Locate every malaria parasite and every leukocyte.
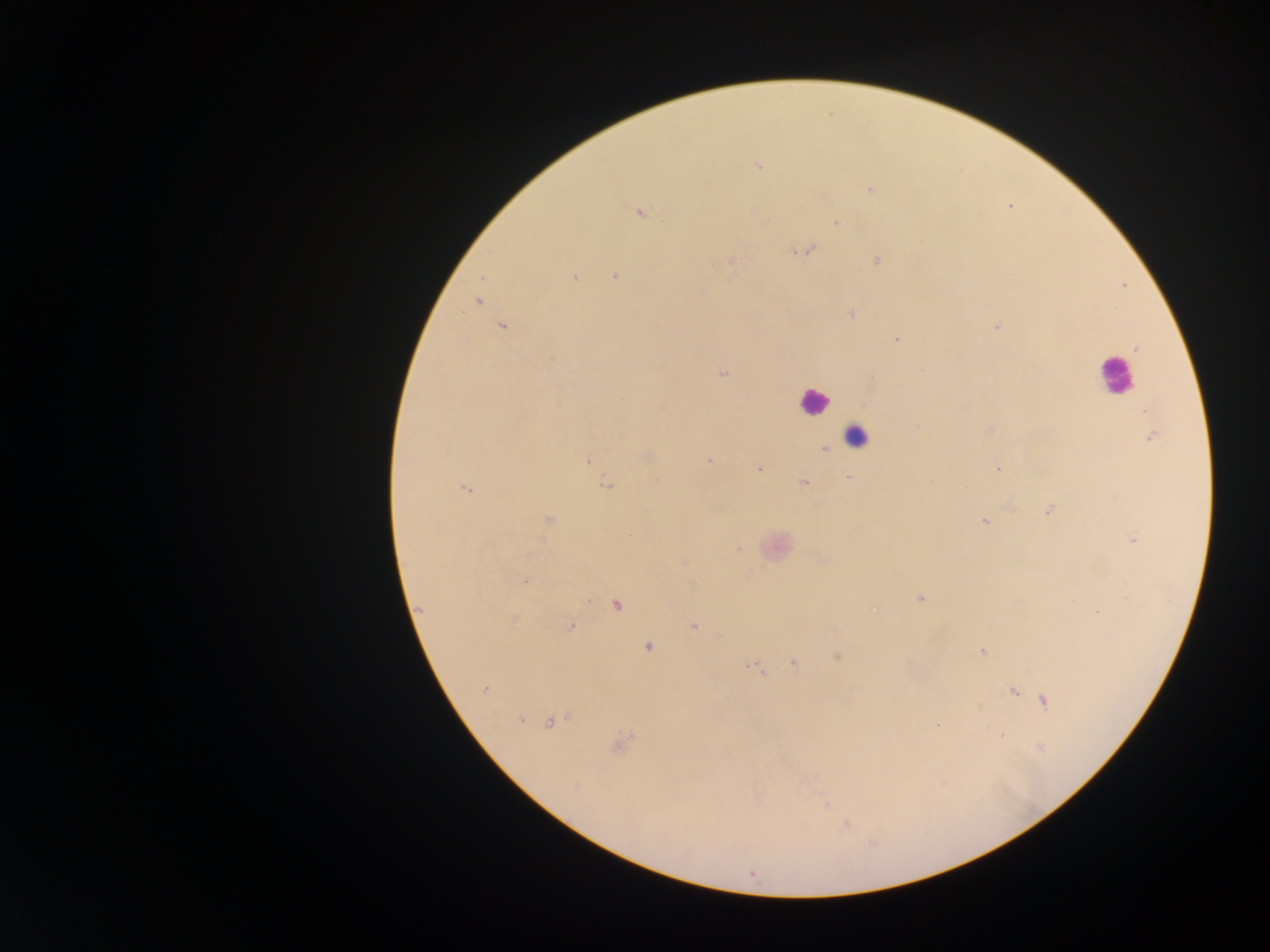
Approximate centers as x y in pixels.
Malaria parasites: 759 166; 870 189; 639 211; 763 221; 835 223; 808 250; 877 261; 729 262; 615 276; 574 277; 478 302; 851 313; 996 326; 502 327; 897 339; 1136 350; 723 374; 871 378; 621 398; 1145 411; 918 427; 1151 437; 824 449; 648 456; 588 461; 707 461; 759 469; 998 469; 848 477; 804 483; 607 486; 466 488; 1047 511; 549 519; 984 522; 1134 541; 738 549; 526 556; 525 581; 920 598; 617 605; 420 609; 1097 612; 694 626; 571 627; 648 646; 983 652; 837 657; 793 663; 754 668; 485 689; 1013 692; 1044 700; 521 720; 551 721; 1001 737; 622 743; 575 785; 825 802; 846 825; 752 874.
Leukocytes: 1115 375; 813 402; 856 437.

Summary:
  - Country: Ghana
  - Preparation: thick blood film
  - Image size: 1270×952 pixels
  - Capture: mobile-phone photograph through a microscope
  - Field of view: single